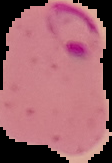

image size = 112×163 pixels
image type = cell region segmented out of the field of view; surrounding area masked to black
preparation = thin blood film
malaria status = parasitized